Assess the morphology of the red blood cells.
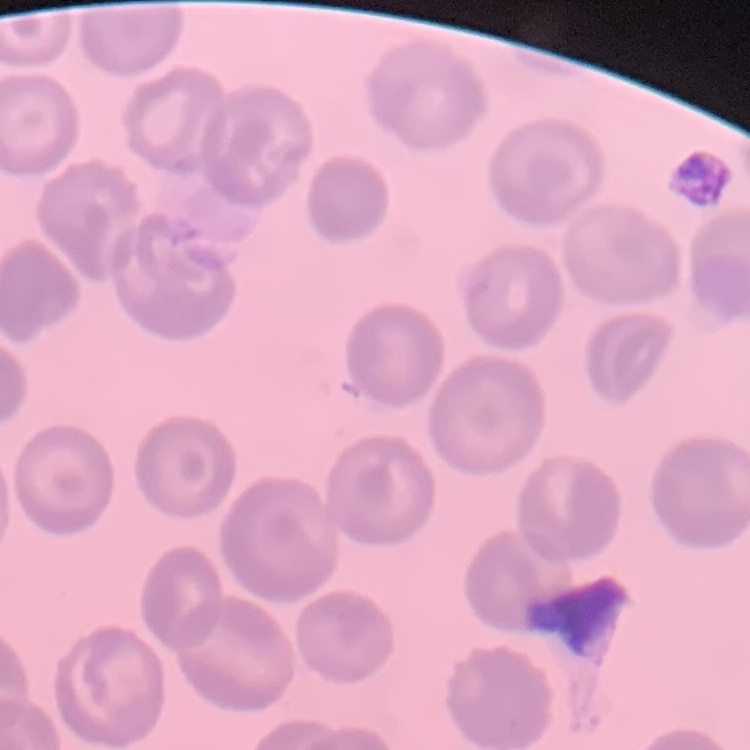
They show no rouleaux formation.

preparation = thin blood film
stain = Field's or Giemsa
image type = one tile cut from a larger photomicrograph